Report the malaria status of this cell.
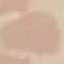
It is uninfected.

Thin smear of blood. Giemsa-stained preparation. Cell patch, automatically extracted from a larger field of view and resized to 64 × 64 pixels. Acquired by smartphone through the microscope eyepiece.